Assess this cell for malaria.
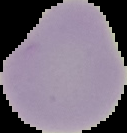
It is uninfected.

From a thin blood film. Cell region segmented out of the field of view; the surrounding area is masked to black. Image is 127×133 pixels.